Report the malaria status of this cell.
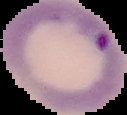
Parasitized.

image_size: 127×115 pixels
image_type: cell region segmented out of the field of view; surrounding area masked to black
preparation: thin blood film